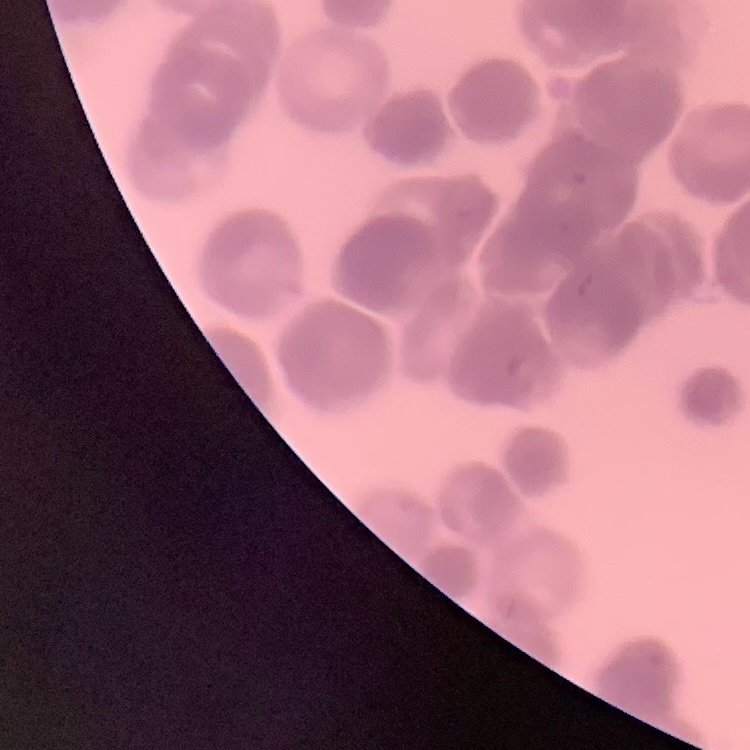
Summary:
  - Red blood cell morphology: rouleaux formation
  - Image type: one tile cut from a larger photomicrograph
  - Preparation: thin blood smear
  - Stain: Field's or Giemsa